Assess the morphology of the red blood cells.
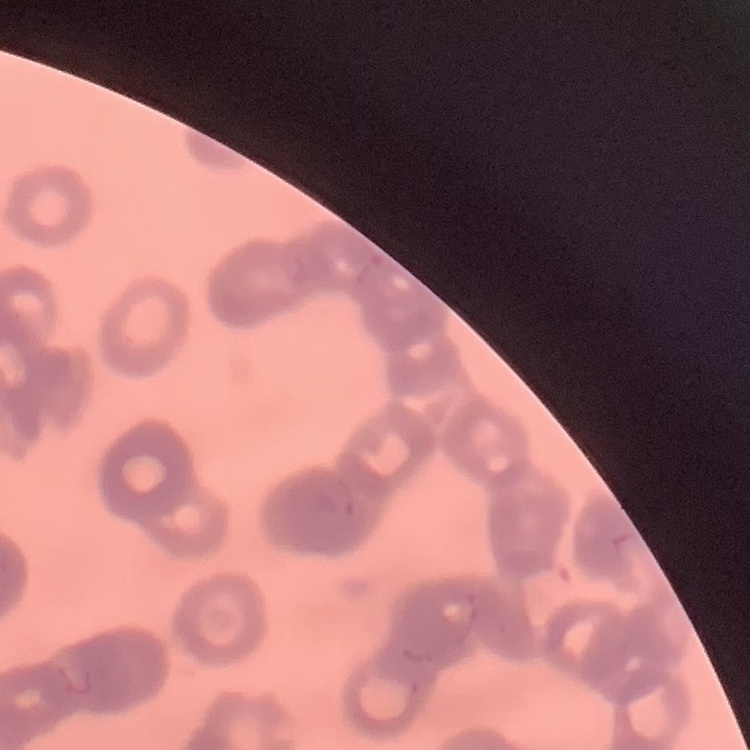
They show rouleaux formation.

Thin peripheral smear. Field's or Giemsa stain. One tile cut from a larger photomicrograph.